Report the malaria status of this cell.
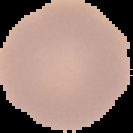
Uninfected.

image size = 133×133 pixels
image type = cell region segmented out of the field of view; surrounding area masked to black
preparation = thin blood smear